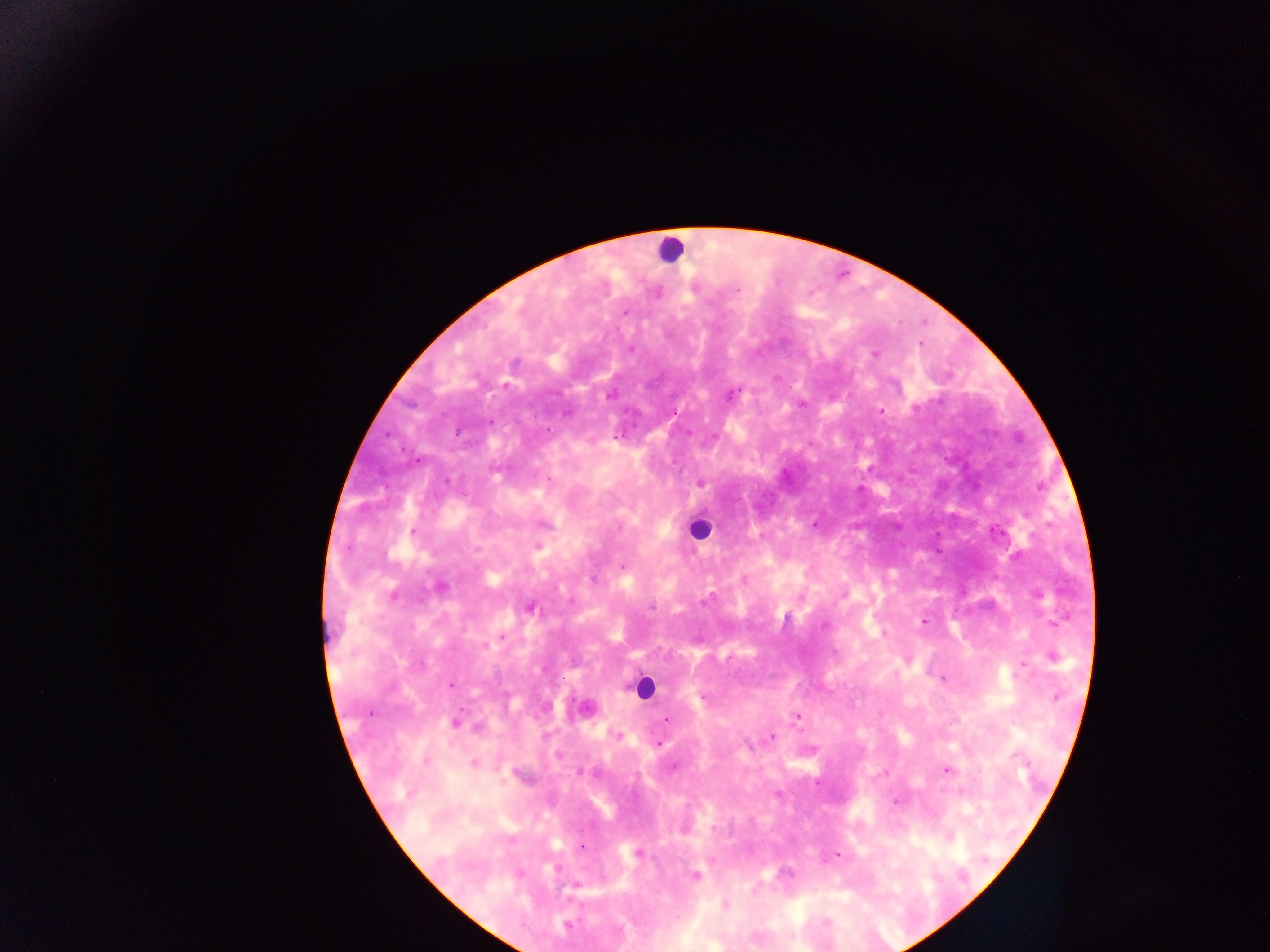

Approximate centers as x y in pixels.
Summary:
  - Malaria parasite locations: 736 290; 626 312; 630 349; 505 386; 609 395; 730 395; 802 405; 881 411; 567 413; 491 421; 548 430; 458 432; 617 437; 700 483; 814 524; 619 527; 412 532; 537 546; 622 566; 744 580; 440 587; 393 595; 570 601; 705 602; 651 607; 531 608; 923 622; 1055 624; 824 625; 884 633; 503 637; 486 646; 1053 656; 1023 665; 942 678; 450 684; 1055 697; 797 717; 666 720; 455 722; 617 736; 772 737; 659 744; 425 761; 474 763; 673 768; 947 770; 895 802; 713 828; 582 847; 637 853; 837 854; 521 874; 695 876; 725 905; 567 925
  - Leukocyte locations: 670 250; 698 529; 643 686
  - Field of view: single
  - Country: Ghana
  - Preparation: thick blood smear
  - Capture: mobile-phone photograph through a microscope
  - Image size: 1270×952 pixels